Locate every malaria parasite.
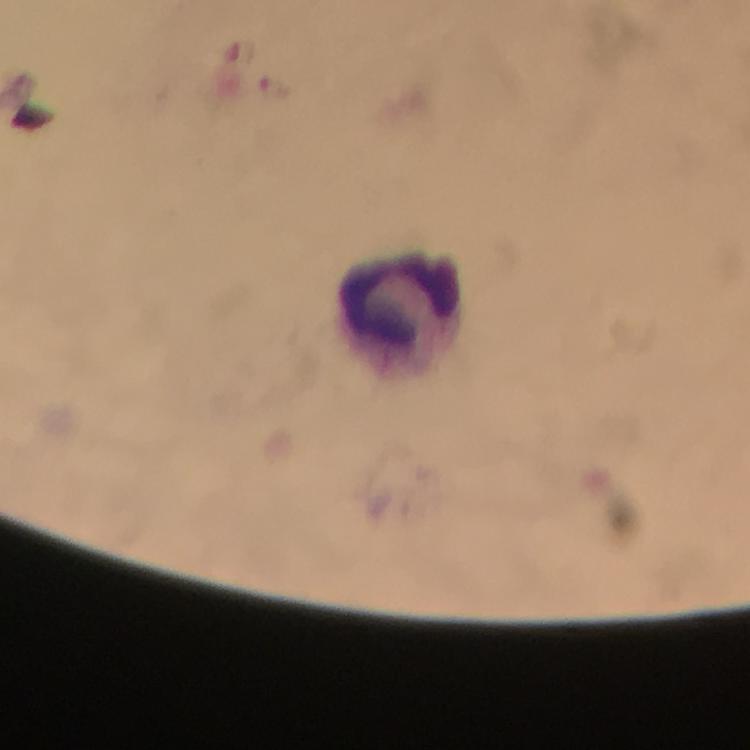

No malaria parasites seen.

Approximate object centers, in pixels from the top-left corner.
Summary:
  - Leukocyte locations: (x=398, y=297)
  - Image size: 750×750 pixels
  - Stain: Giemsa
  - Capture: smartphone camera through the microscope
  - Cropped from: a single field of view
  - Magnification: 100x
  - Immersion oil: applied
  - Context: from a diagnostic examination for malaria
  - Preparation: thick smear